Evaluate for Plasmodium parasites.
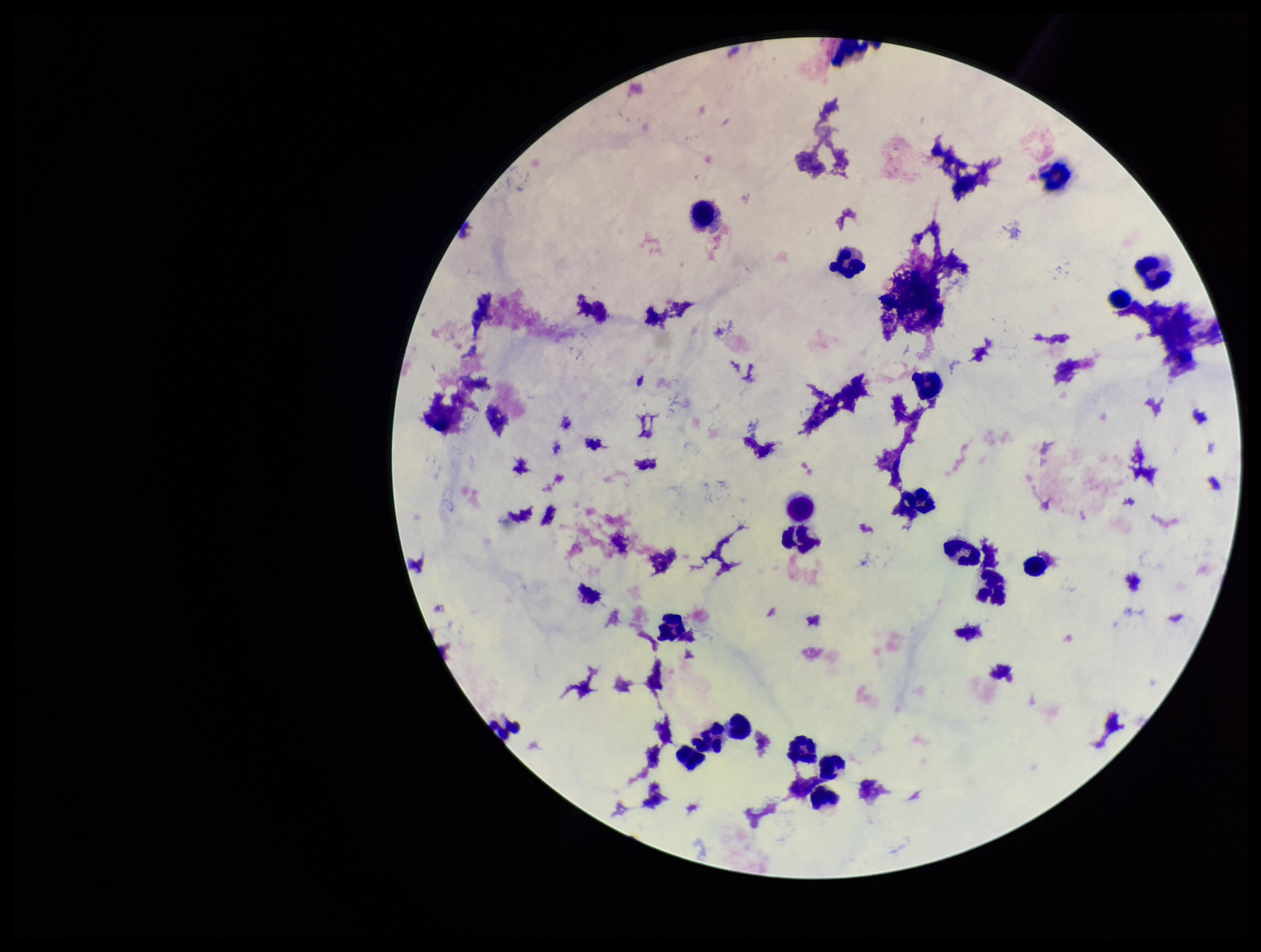
None seen.

{
  "parasite_count": 0,
  "stain": "Giemsa",
  "field_of_view": "one from this slide",
  "capture": "smartphone photograph through the microscope eyepiece",
  "image_size": "1261×952 pixels",
  "preparation": "thick blood smear",
  "leukocyte_count": 19,
  "patient_malaria_status": "negative"
}